State which parasite is depicted.
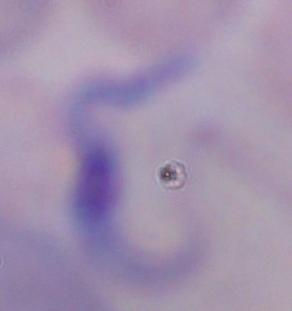

A trypanosome.

Micrograph. Captured at 1000x magnification.